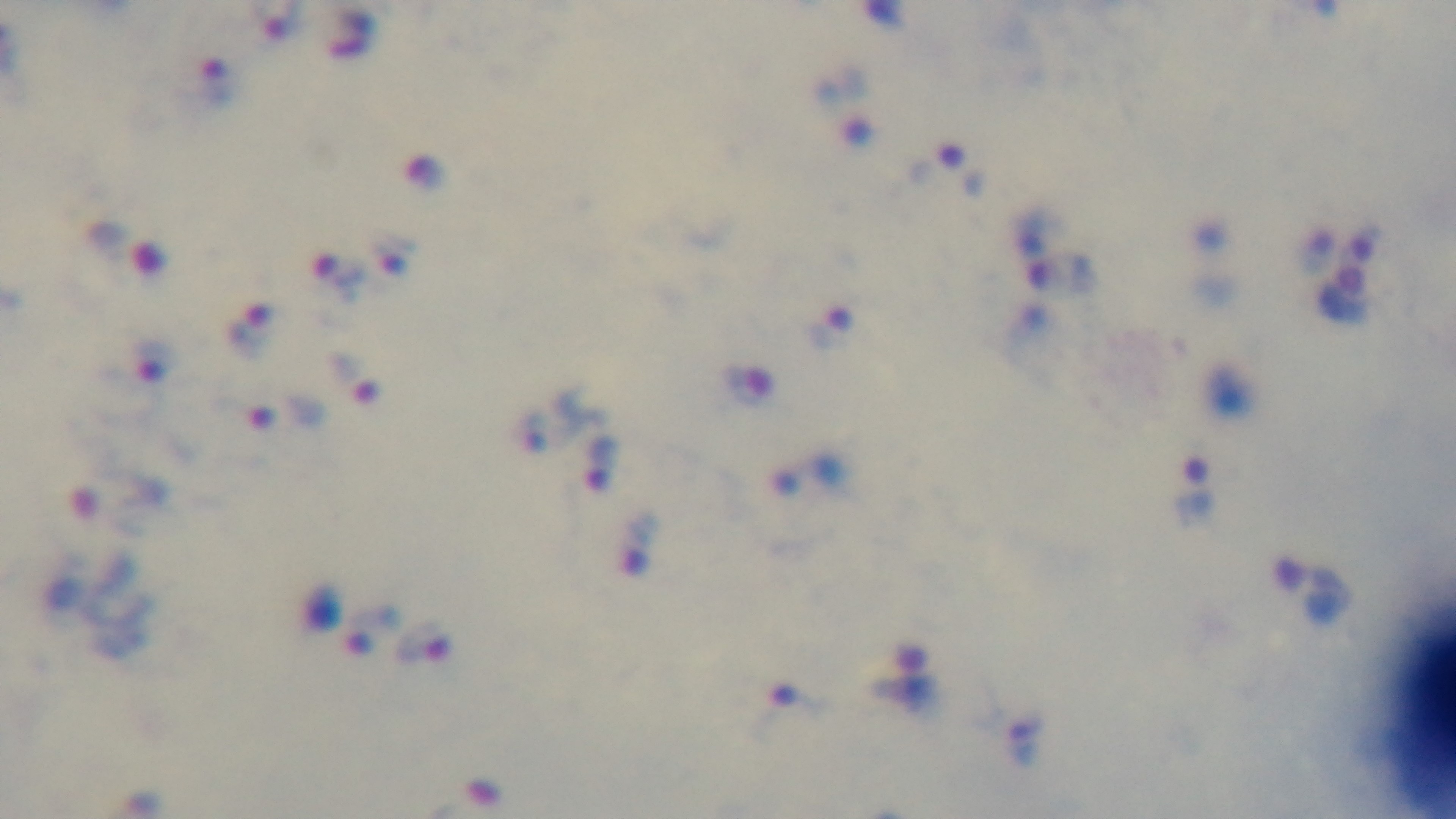
Summary:
  - Stain: Giemsa
  - Field of view: one from the slide
  - Malaria status: positive
  - Capture: mounted 4K digital camera
  - Objective: 100x oil immersion
  - Preparation: thick
  - Modality: light microscopy